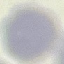
malaria status = uninfected
preparation = thin blood film
stain = Giemsa
image type = cell patch, automatically extracted from a larger field of view and resized to 64 × 64 pixels
capture = smartphone camera at the microscope eyepiece